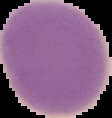
result: no malaria parasites seen
preparation: thin blood smear
image_type: segmented cell region on a black background
image_size: 112×118 pixels